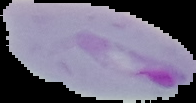
Segmented cell region on a black background. From a thin blood film. Image is 196×103 pixels. Malaria status: parasitized.